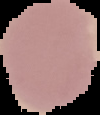

Summary:
  - Result: no Plasmodium parasites seen
  - Preparation: thin blood smear
  - Image size: 100×115 pixels
  - Image type: cell region segmented out of the field of view; surrounding area masked to black